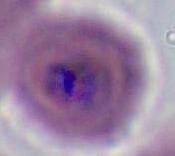

Photomicrograph. Captured at either 400x or 1000x magnification. A Plasmodium parasite is seen.